Outline each blood parasite and name the species.
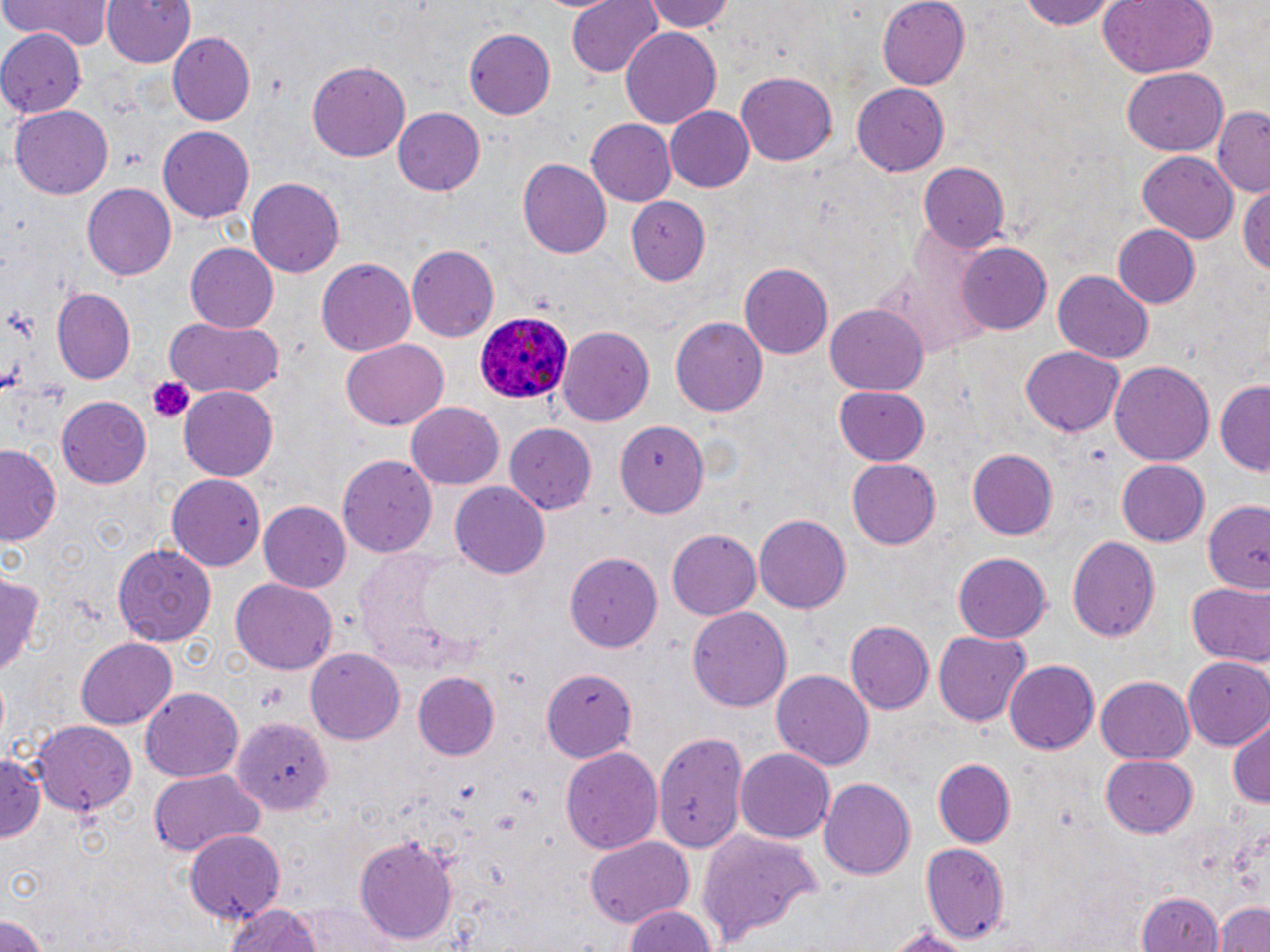
Approximate bounding boxes as named x1/y1/x2/y2 corners in pixels.
Plasmodium ovale-infected red blood cells: (x1=474, y1=312, x2=573, y2=404).
No Plasmodium falciparum, Plasmodium malariae, Plasmodium vivax, Babesia divergens, or Trypanosoma brucei observed.

slide-level diagnosis = Plasmodium ovale
platelet locations = approximate bounding boxes as named x1/y1/x2/y2 corners in pixels: (x1=119, y1=141, x2=146, y2=173), (x1=146, y1=378, x2=194, y2=423)
stain = May-Grünwald-Giemsa
preparation = thin blood smear
magnification = 1000x
modality = optical microscopy
uninfected red blood cell locations = approximate bounding boxes as named x1/y1/x2/y2 corners in pixels: (x1=2, y1=0, x2=112, y2=51), (x1=97, y1=0, x2=198, y2=69), (x1=566, y1=0, x2=664, y2=76), (x1=643, y1=0, x2=735, y2=32), (x1=877, y1=0, x2=971, y2=90), (x1=1018, y1=0, x2=1122, y2=28), (x1=1095, y1=0, x2=1217, y2=78), (x1=619, y1=24, x2=722, y2=126), (x1=0, y1=27, x2=86, y2=117), (x1=463, y1=28, x2=557, y2=118), (x1=168, y1=32, x2=256, y2=126), (x1=307, y1=59, x2=410, y2=160), (x1=1122, y1=69, x2=1227, y2=154), (x1=734, y1=72, x2=836, y2=166), (x1=852, y1=82, x2=949, y2=176), (x1=10, y1=105, x2=112, y2=199), (x1=664, y1=106, x2=753, y2=191), (x1=393, y1=107, x2=484, y2=196), (x1=1213, y1=109, x2=1268, y2=196), (x1=586, y1=119, x2=676, y2=205), (x1=157, y1=127, x2=254, y2=222), (x1=1137, y1=151, x2=1238, y2=244), (x1=518, y1=156, x2=610, y2=258), (x1=917, y1=162, x2=1008, y2=251), (x1=247, y1=176, x2=345, y2=276), (x1=1240, y1=182, x2=1270, y2=280), (x1=83, y1=183, x2=176, y2=281), (x1=623, y1=197, x2=711, y2=288), (x1=1110, y1=224, x2=1199, y2=310), (x1=956, y1=242, x2=1053, y2=334), (x1=185, y1=244, x2=279, y2=331), (x1=407, y1=244, x2=499, y2=343), (x1=317, y1=256, x2=418, y2=356), (x1=738, y1=263, x2=832, y2=360), (x1=1053, y1=268, x2=1153, y2=361), (x1=51, y1=287, x2=136, y2=384), (x1=825, y1=305, x2=930, y2=394), (x1=165, y1=316, x2=286, y2=399), (x1=671, y1=317, x2=769, y2=417), (x1=559, y1=326, x2=655, y2=428), (x1=341, y1=339, x2=448, y2=430), (x1=1020, y1=346, x2=1124, y2=437), (x1=1110, y1=362, x2=1215, y2=466), (x1=1215, y1=378, x2=1270, y2=474), (x1=834, y1=384, x2=929, y2=465), (x1=180, y1=386, x2=278, y2=481), (x1=57, y1=396, x2=152, y2=488), (x1=407, y1=402, x2=503, y2=490), (x1=615, y1=422, x2=710, y2=519), (x1=506, y1=423, x2=598, y2=515), (x1=1, y1=444, x2=63, y2=547), (x1=967, y1=448, x2=1059, y2=540), (x1=338, y1=454, x2=436, y2=558), (x1=847, y1=457, x2=941, y2=549), (x1=1117, y1=460, x2=1209, y2=544), (x1=167, y1=471, x2=264, y2=569), (x1=450, y1=482, x2=549, y2=579), (x1=1201, y1=500, x2=1270, y2=595), (x1=260, y1=502, x2=351, y2=593), (x1=754, y1=514, x2=850, y2=616), (x1=667, y1=529, x2=761, y2=619), (x1=1066, y1=536, x2=1160, y2=643), (x1=111, y1=541, x2=215, y2=646), (x1=355, y1=550, x2=501, y2=673), (x1=565, y1=552, x2=663, y2=651), (x1=953, y1=552, x2=1051, y2=642), (x1=0, y1=572, x2=43, y2=679), (x1=229, y1=578, x2=337, y2=675), (x1=1186, y1=580, x2=1269, y2=667), (x1=688, y1=608, x2=791, y2=715), (x1=845, y1=621, x2=935, y2=714), (x1=932, y1=630, x2=1031, y2=726), (x1=75, y1=638, x2=176, y2=727), (x1=305, y1=646, x2=406, y2=744), (x1=1184, y1=658, x2=1270, y2=749), (x1=1004, y1=660, x2=1101, y2=755), (x1=772, y1=670, x2=875, y2=769), (x1=543, y1=671, x2=637, y2=764), (x1=412, y1=673, x2=497, y2=759), (x1=1095, y1=674, x2=1196, y2=763), (x1=142, y1=686, x2=244, y2=782), (x1=1228, y1=716, x2=1270, y2=809), (x1=234, y1=717, x2=331, y2=816), (x1=31, y1=719, x2=139, y2=814), (x1=653, y1=734, x2=749, y2=852), (x1=562, y1=746, x2=662, y2=858), (x1=735, y1=747, x2=835, y2=842), (x1=0, y1=750, x2=45, y2=844), (x1=1100, y1=753, x2=1197, y2=837), (x1=932, y1=756, x2=1016, y2=847), (x1=149, y1=770, x2=264, y2=857), (x1=820, y1=779, x2=915, y2=880), (x1=184, y1=829, x2=285, y2=922), (x1=697, y1=829, x2=822, y2=947), (x1=353, y1=836, x2=459, y2=944), (x1=584, y1=837, x2=694, y2=928), (x1=921, y1=843, x2=1008, y2=945), (x1=1137, y1=890, x2=1223, y2=952), (x1=225, y1=902, x2=323, y2=952), (x1=1218, y1=902, x2=1270, y2=952), (x1=309, y1=903, x2=405, y2=952), (x1=622, y1=904, x2=722, y2=952), (x1=0, y1=911, x2=50, y2=950), (x1=883, y1=924, x2=979, y2=952)
image size = 1270×952 pixels
field of view = single